Assess this cell for malaria.
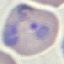

It is parasitized.

Thin smear of blood. Cell patch, automatically extracted from a larger field of view and resized to 64 × 64 pixels. Acquired by smartphone through the microscope eyepiece. Giemsa-stained preparation.